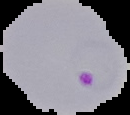 Image is 130×115 pixels. Result: Plasmodium parasites identified. From a thin blood smear. The area outside the segmented cell region is set to black.